Identify the parasite.
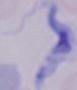

A trypanosome.

{
  "modality": "photomicrograph",
  "magnification": "1000x"
}